Report the malaria status of this cell.
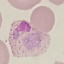

Parasitized.

Summary:
  - Image type: automatically extracted cell patch, resized to 64 × 64 pixels
  - Capture: smartphone camera at the microscope eyepiece
  - Preparation: thin blood smear
  - Stain: Giemsa